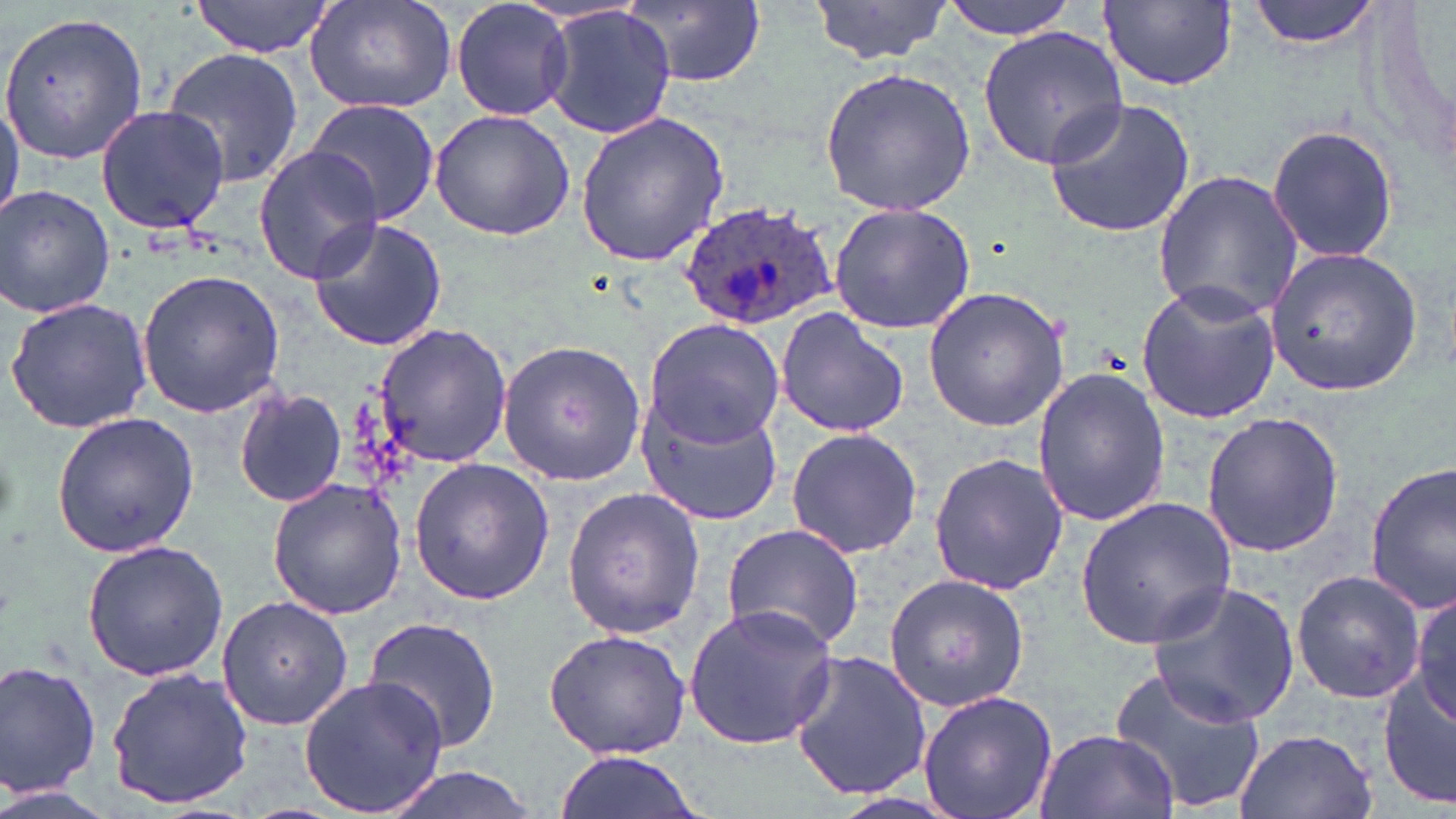

slide-level diagnosis = Plasmodium ovale
uninfected red blood cell locations = approximate bounding boxes as (x1, y1, x2, y2) in pixels: (190, 0, 337, 56), (450, 0, 573, 122), (623, 0, 769, 89), (807, 0, 954, 65), (941, 0, 1079, 38), (1245, 0, 1385, 50), (1096, 1, 1240, 94), (305, 2, 455, 115), (540, 6, 676, 139), (0, 11, 149, 166), (977, 24, 1130, 170), (160, 47, 303, 188), (818, 67, 977, 218), (0, 87, 23, 223), (1043, 95, 1196, 237), (305, 99, 440, 226), (95, 103, 231, 236), (429, 109, 574, 242), (575, 110, 730, 266), (1267, 123, 1398, 264), (253, 145, 384, 283), (1153, 168, 1305, 324), (0, 184, 117, 320), (828, 204, 975, 336), (307, 214, 448, 354), (1262, 245, 1424, 398), (135, 268, 288, 419), (1135, 281, 1282, 424), (922, 285, 1070, 432), (4, 293, 156, 436), (773, 308, 911, 437), (641, 319, 785, 448), (373, 323, 515, 469), (495, 339, 646, 485), (1032, 367, 1171, 530), (232, 385, 348, 508), (637, 394, 783, 528), (50, 411, 199, 559), (1203, 412, 1343, 556), (784, 426, 923, 559), (927, 451, 1068, 595), (408, 458, 554, 604), (1366, 462, 1456, 613), (266, 475, 409, 620), (561, 486, 705, 639), (1074, 496, 1239, 650), (718, 522, 865, 653), (81, 538, 228, 681), (1291, 571, 1427, 703), (882, 572, 1029, 713), (1147, 580, 1302, 730), (1409, 592, 1456, 731), (215, 594, 351, 731), (681, 603, 841, 751), (362, 615, 503, 755), (542, 628, 693, 760), (786, 650, 935, 802), (0, 660, 102, 797), (1105, 661, 1265, 817), (1377, 663, 1456, 811), (106, 667, 254, 810), (298, 675, 447, 815), (915, 689, 1060, 819), (1034, 728, 1177, 819), (1233, 728, 1376, 819), (554, 750, 704, 819), (373, 765, 545, 819), (0, 785, 120, 819)
image size = 1456×819 pixels
magnification = 1000x
field of view = single
preparation = thin blood smear
modality = optical microscopy
Plasmodium ovale-infected red blood cell locations = approximate bounding boxes as (x1, y1, x2, y2) in pixels: (675, 200, 843, 332)
stain = May-Grünwald-Giemsa